Locate every malaria parasite.
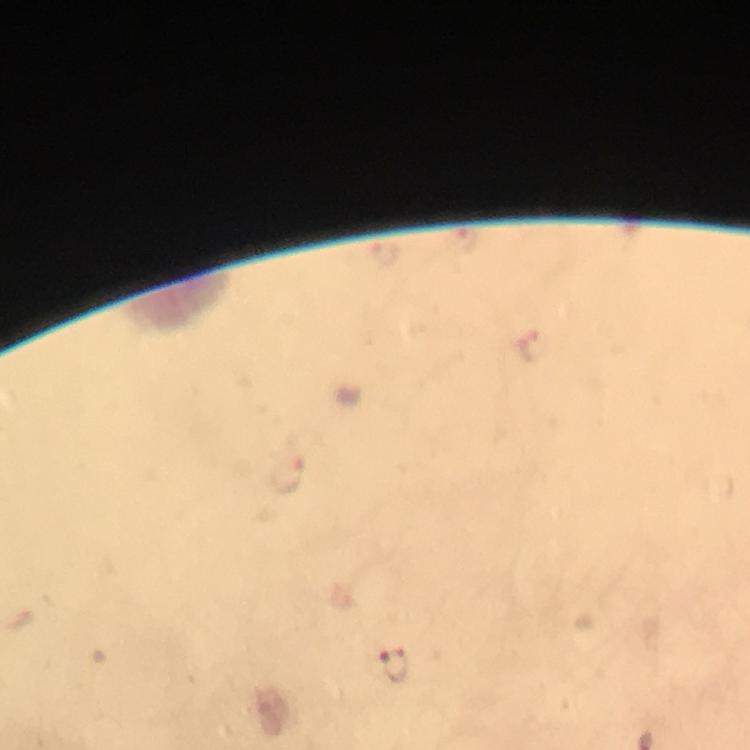

Approximate centers as (x, y) in pixels.
Malaria parasites: (467, 240), (386, 253), (526, 344), (391, 664).

Summary:
  - Context: from a diagnostic examination for malaria
  - Capture: smartphone mounted on the microscope
  - Preparation: thick blood smear
  - Image size: 750×750 pixels
  - Stain: Giemsa
  - Cropped from: a single field of view
  - Magnification: 100x
  - Immersion oil: used